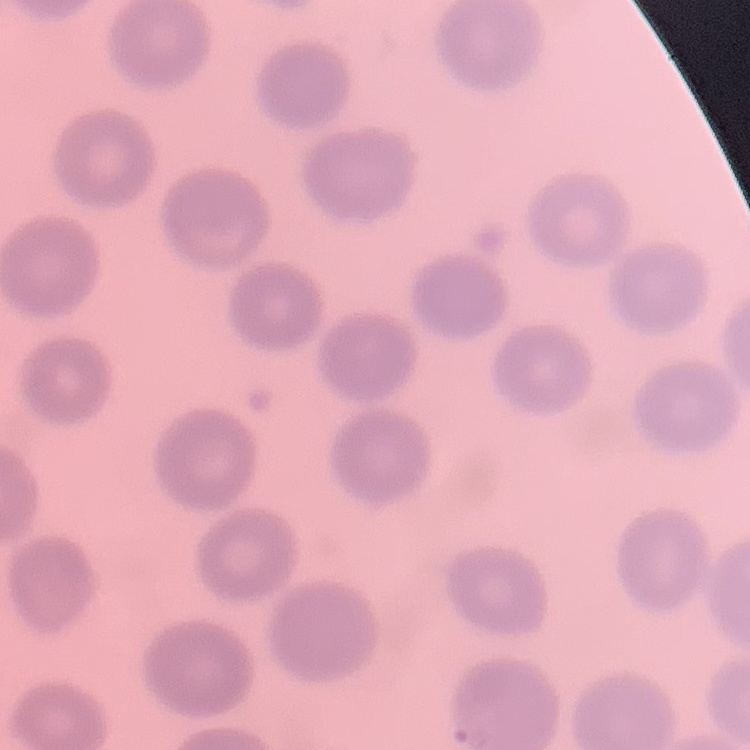

Summary:
  - Erythrocyte morphology: no rouleaux formation
  - Image type: square crop of a larger photomicrograph
  - Preparation: thin blood film
  - Stain: Field's or Giemsa